Identify the parasite.
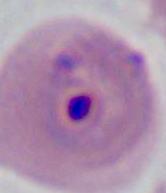

Plasmodium.

magnification: 400x or 1000x
modality: micrograph